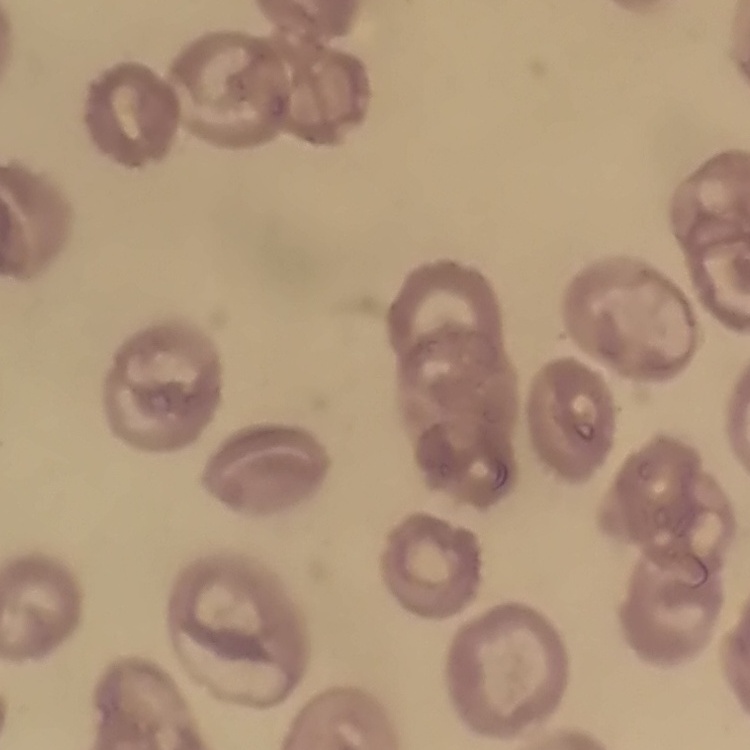 The red blood cells show no rouleaux formation. Square crop of a larger photomicrograph. Stained with either Field's or Giemsa. Thin blood smear.